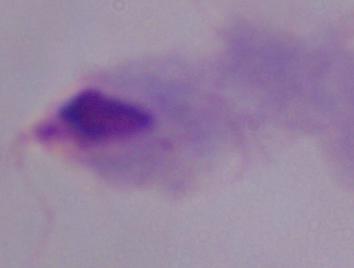
{
  "magnification": "1000x",
  "identification": "trichomonad",
  "modality": "photomicrograph"
}